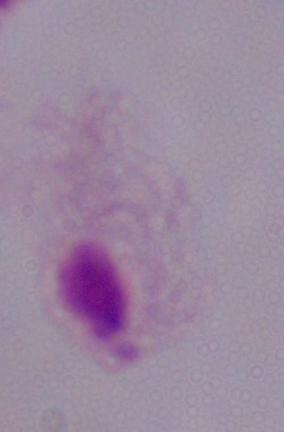
Micrograph. 1000x magnification. A trichomonad is shown.